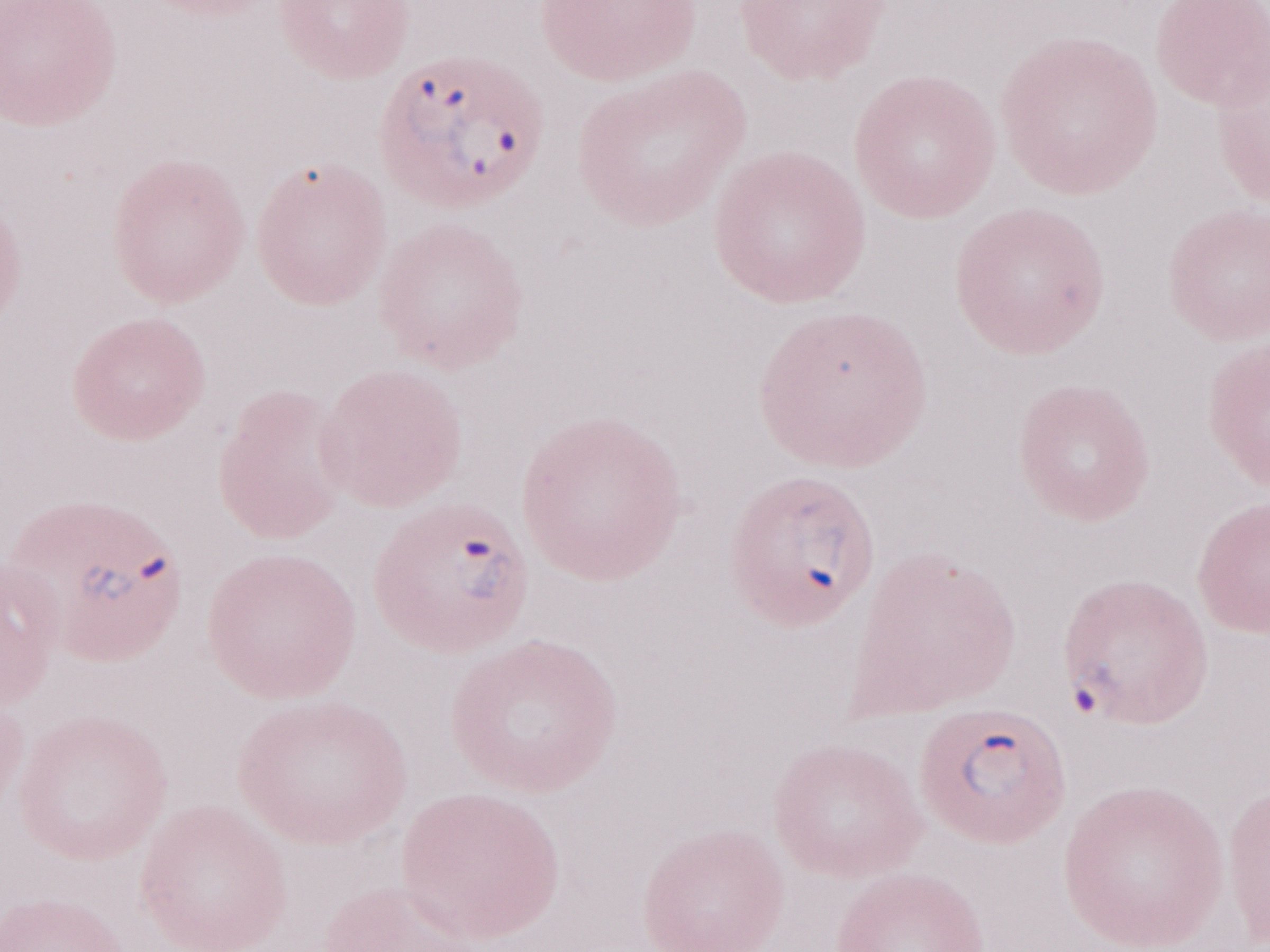 Magnification: 1,000x. Patient-level malaria diagnosis: positive. Image is 1270×952 pixels. One field of this slide. Thin blood smear. Olympus BX43 microscope, Olympus DP73 camera. May-Grünwald-Giemsa-stained preparation.